Assess this cell for malaria.
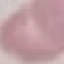
It is uninfected.

Giemsa stain. Acquired by smartphone through the microscope eyepiece. Automatically extracted cell patch, resized to 64 × 64 pixels. Thin smear of blood.